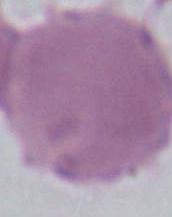
Summary:
  - Identification: erythrocyte
  - Magnification: 1000x
  - Modality: photomicrograph